State which cell type is depicted.
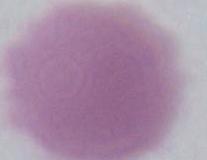
An erythrocyte.

Photomicrograph. Captured at 1000x magnification.